Describe the morphology of the erythrocytes.
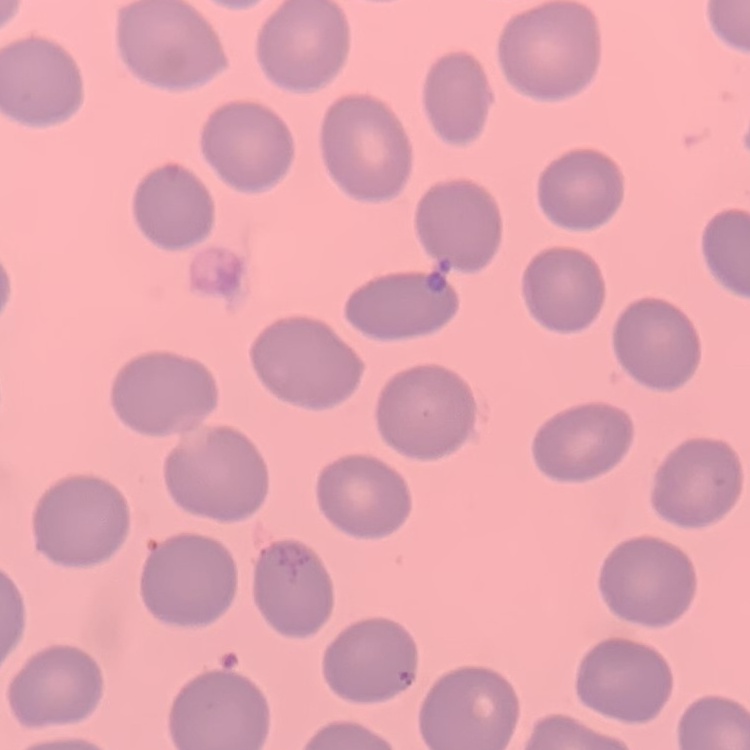

They show no rouleaux formation.

Summary:
  - Image type: square crop of a larger photomicrograph
  - Preparation: thin blood smear
  - Stain: Field's or Giemsa